Assess this cell for malaria.
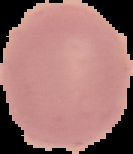

Uninfected.

image size = 133×154 pixels
preparation = thin blood film
image type = segmented cell region on a black background